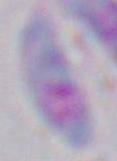
magnification: 1000x
modality: photomicrograph
identification: Toxoplasma gondii